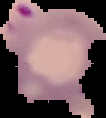

The area outside the segmented cell region is set to black. Image is 106×118 pixels. From a thin blood film. Malaria status: parasitized.